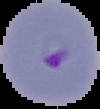
Summary:
  - Result: malaria parasites detected
  - Image size: 100×109 pixels
  - Image type: segmented cell region with the area outside set to black
  - Preparation: thin blood smear